Report the malaria status of this cell.
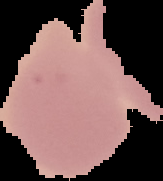
Uninfected.

preparation = thin blood film
image type = cell region segmented out of the field of view; surrounding area masked to black
image size = 163×181 pixels